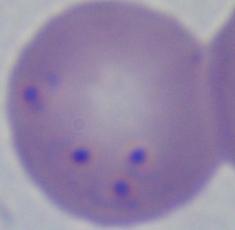
A Babesia parasite is shown. 1000x magnification. Micrograph.